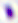

Micrograph. Toxoplasma gondii is shown. 400x magnification.